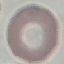

result: no malaria parasites detected
preparation: thin smear
capture: smartphone camera at the microscope eyepiece
image_type: cell patch, automatically extracted from a larger field of view and resized to 64 × 64 pixels
stain: Giemsa